Describe the morphology of the erythrocytes.
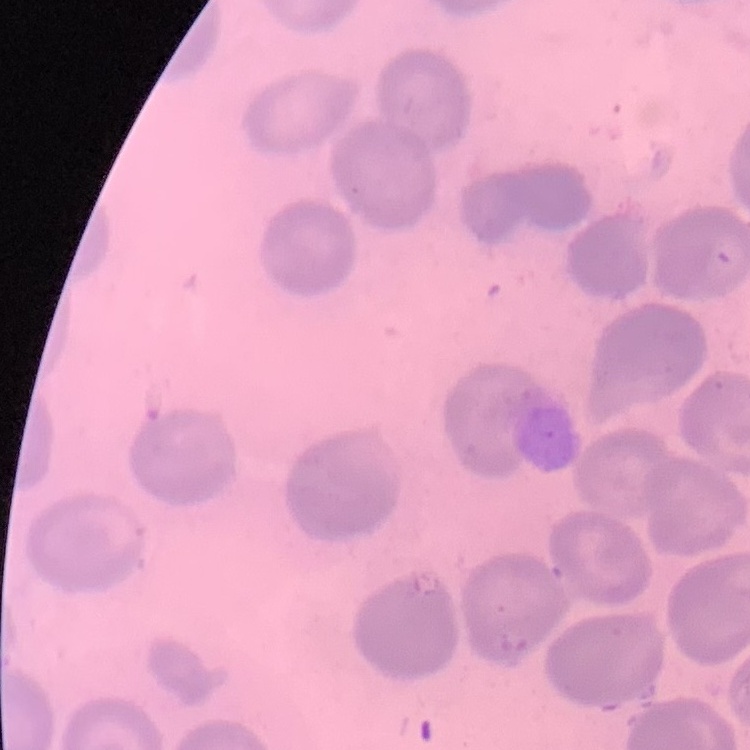

No rouleaux formation.

One tile cut from a larger photomicrograph. Stained with either Field's or Giemsa. Thin blood smear.